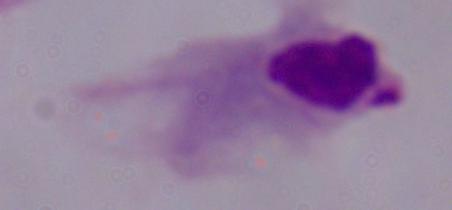
1000x magnification. Micrograph. A trichomonad is seen.